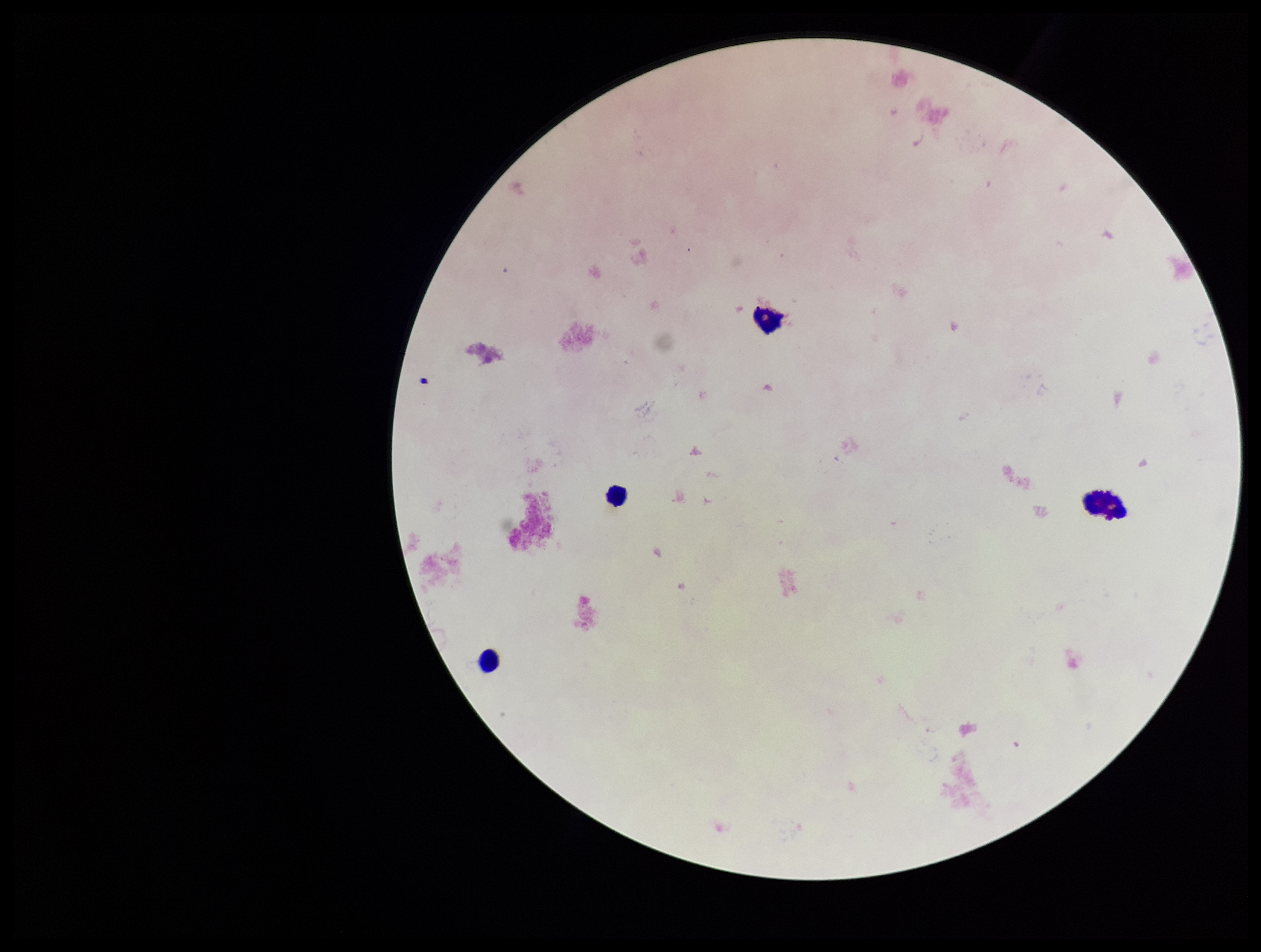

parasite count = 0
Plasmodium parasites = none seen
leukocyte count = 4
preparation = thick smear
patient malaria status = negative
image size = 1261×952 pixels
field of view = single
stain = Giemsa
capture = smartphone photograph through the microscope eyepiece